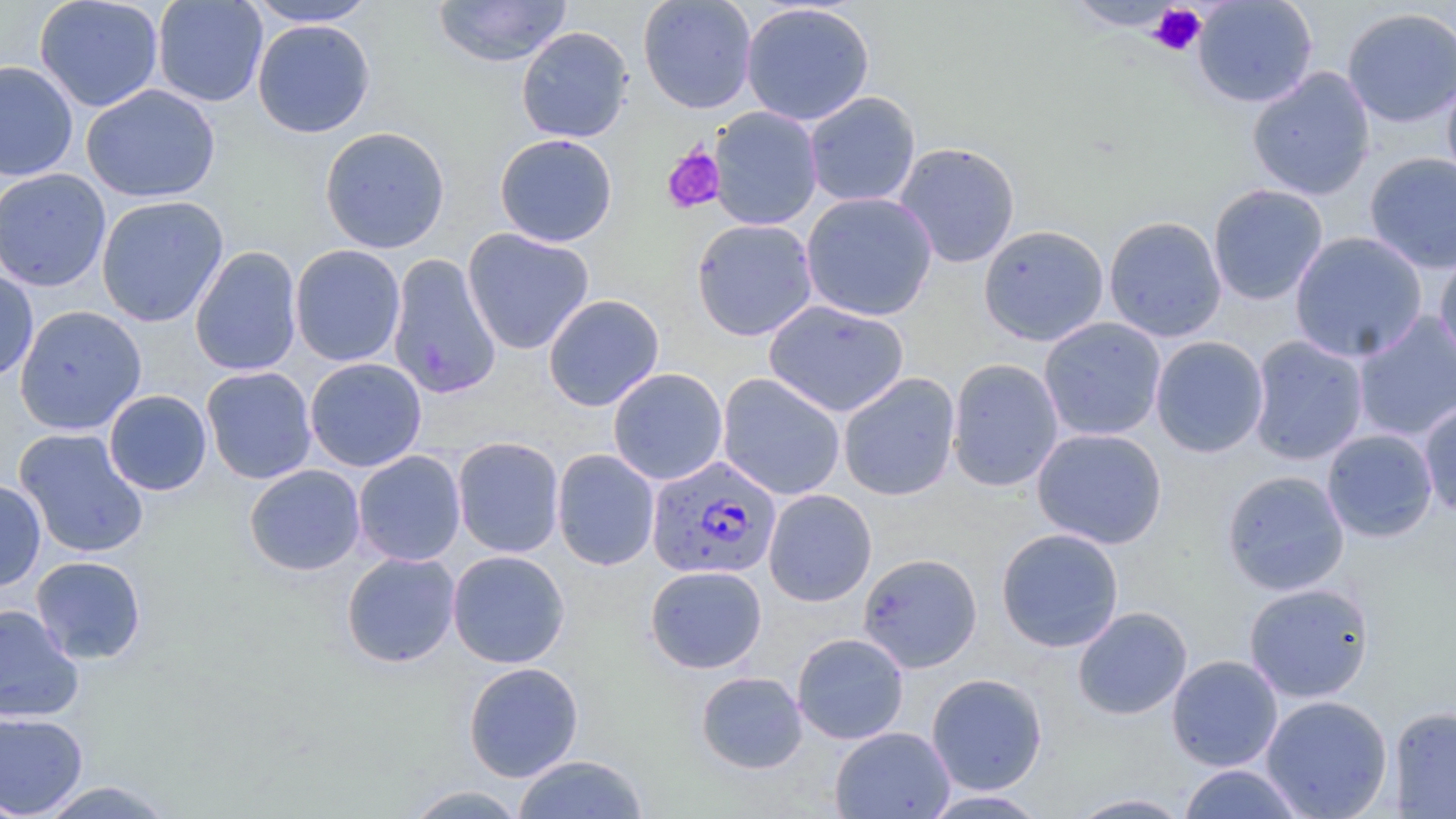
Approximate bounding boxes as (x1,y1)-(x2,y2) corner pairs in pixels. Platelet locations: (1149,4)-(1207,56), (662,145)-(726,214). Plasmodium falciparum-infected red blood cell locations: (646,454)-(782,580). Uninfected red blood cell locations: (33,0)-(164,112), (153,0)-(268,107), (243,0)-(380,26), (433,0)-(572,67), (637,0)-(758,114), (1192,0)-(1319,108), (1063,1)-(1187,31), (740,2)-(875,126), (1341,7)-(1456,128), (252,18)-(376,138), (516,26)-(634,143), (0,61)-(79,182), (1246,67)-(1375,200), (1441,71)-(1456,189), (80,84)-(220,203), (804,91)-(921,208), (708,106)-(823,231), (319,126)-(451,254), (494,133)-(618,247), (894,141)-(1020,269), (1364,152)-(1456,274), (0,168)-(112,292), (1208,183)-(1328,306), (801,191)-(938,321), (96,195)-(228,328), (1103,215)-(1227,342), (691,218)-(818,341), (978,224)-(1109,346), (462,228)-(595,354), (1289,231)-(1428,363), (290,244)-(406,367), (190,246)-(303,376), (1435,247)-(1456,368), (387,253)-(502,399), (0,269)-(39,382), (543,294)-(664,412), (764,299)-(909,417), (14,305)-(146,435), (1352,311)-(1455,443), (1039,317)-(1167,441), (1150,336)-(1269,458), (1247,336)-(1370,465), (304,357)-(427,472), (947,358)-(1064,492), (201,366)-(317,484), (608,368)-(728,485), (717,373)-(846,500), (838,373)-(961,501), (103,390)-(212,495), (1418,399)-(1456,517), (14,428)-(149,558), (1032,428)-(1167,549), (1321,429)-(1439,543), (452,437)-(564,558), (552,449)-(660,571), (353,450)-(466,566), (244,464)-(366,576), (1221,470)-(1350,596), (0,479)-(46,591), (763,489)-(877,606), (996,528)-(1124,652), (447,550)-(570,668), (341,551)-(461,668), (858,553)-(983,672), (31,556)-(147,664), (645,565)-(767,673), (1243,581)-(1375,703), (0,603)-(85,723), (1073,606)-(1192,720), (792,633)-(909,744), (1166,655)-(1283,771), (462,662)-(584,782), (696,671)-(807,774), (926,673)-(1048,795), (1260,694)-(1393,819), (1389,706)-(1455,818), (0,712)-(88,817), (830,726)-(955,819), (512,754)-(649,818), (1177,763)-(1307,818), (36,781)-(178,818), (401,784)-(530,818), (919,789)-(1052,818), (1067,793)-(1193,818). Slide-level diagnosis: Plasmodium falciparum. 1000x magnification. May-Grünwald-Giemsa-stained preparation. One field of a larger specimen. Thin blood smear. Image is 1456×819 pixels. Light microscopy.